Assess this cell for malaria.
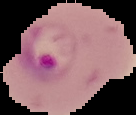
It is parasitized.

From a thin blood smear. Image is 136×115 pixels. Segmented cell region on a black background.